Identify the blood parasite species.
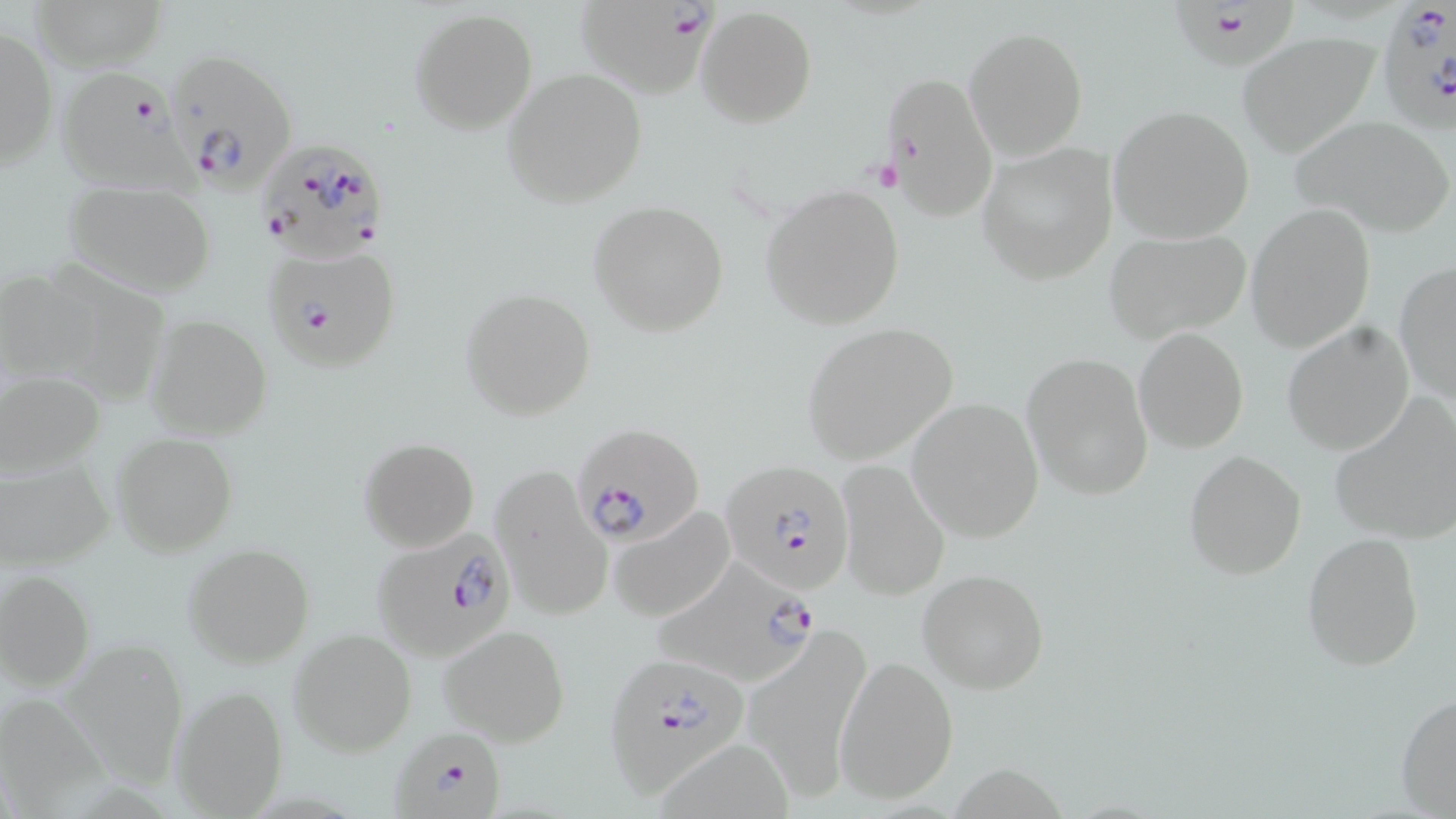

Plasmodium falciparum.

Summary:
  - Coordinate format: approximate bounding boxes as (x1, y1, x2, y2) in pixels
  - Platelet locations: (869, 158, 905, 194)
  - Uninfected red blood cell locations: (30, 0, 166, 70), (697, 6, 818, 128), (410, 8, 536, 135), (1, 20, 57, 174), (963, 26, 1089, 160), (1236, 33, 1380, 157), (501, 68, 648, 208), (880, 69, 998, 221), (1108, 105, 1255, 243), (1291, 115, 1453, 237), (977, 142, 1117, 285), (62, 180, 216, 295), (760, 182, 905, 330), (589, 200, 730, 337), (1245, 203, 1377, 353), (1103, 228, 1252, 346), (55, 249, 181, 406), (1394, 261, 1456, 402), (0, 267, 113, 394), (462, 289, 595, 420), (147, 315, 272, 441), (1282, 321, 1415, 455), (800, 323, 959, 464), (1134, 327, 1250, 452), (1022, 351, 1154, 500), (1, 371, 105, 482), (907, 397, 1045, 542), (1329, 397, 1456, 545), (112, 433, 237, 554), (359, 437, 480, 553), (1184, 450, 1307, 580), (2, 456, 113, 571), (834, 460, 950, 599), (493, 465, 613, 621), (608, 505, 736, 623), (1302, 532, 1424, 671), (182, 542, 315, 667), (918, 568, 1049, 695), (0, 569, 94, 691), (438, 624, 570, 746), (744, 626, 871, 800), (289, 628, 417, 755), (75, 639, 182, 799), (835, 654, 959, 805), (172, 686, 289, 816), (1, 692, 118, 819), (1396, 692, 1456, 818)
  - Plasmodium falciparum-infected red blood cell locations: (1375, 0, 1456, 134), (575, 3, 707, 97), (1166, 4, 1299, 75), (162, 48, 297, 192), (55, 68, 210, 209), (252, 139, 393, 275), (265, 246, 402, 372), (575, 427, 703, 547), (722, 461, 856, 594), (370, 527, 520, 663), (654, 560, 823, 690), (604, 650, 746, 795), (391, 726, 507, 819)
  - Field of view: single
  - Stain: May-Grünwald-Giemsa
  - Preparation: thin blood smear
  - Modality: light microscopy
  - Magnification: 1000x
  - Image size: 1456×819 pixels